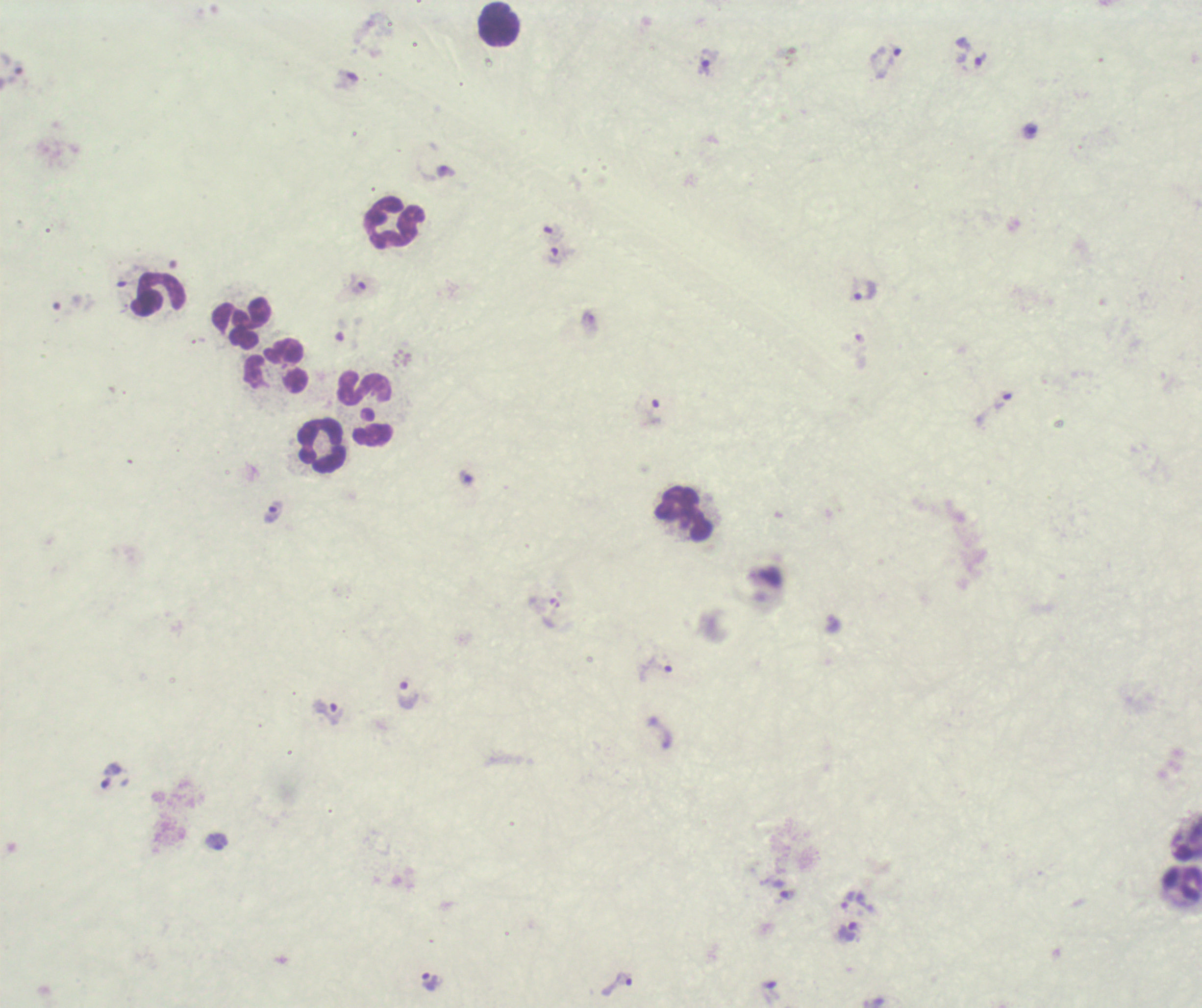
coordinate format = approximate object centers, in pixels from the top-left corner
trophozoite locations = (x=981, y=61), (x=886, y=62), (x=706, y=63), (x=1029, y=131), (x=445, y=172), (x=555, y=255), (x=357, y=285), (x=865, y=290), (x=1002, y=401), (x=651, y=412), (x=466, y=478), (x=273, y=512), (x=656, y=670), (x=407, y=695), (x=329, y=712), (x=111, y=776), (x=216, y=842), (x=787, y=895), (x=847, y=900), (x=847, y=933), (x=430, y=983), (x=617, y=984)
leukocyte locations = (x=498, y=24), (x=394, y=222), (x=156, y=294), (x=241, y=324), (x=275, y=367), (x=363, y=388), (x=373, y=435), (x=323, y=445), (x=684, y=514), (x=1180, y=884)
coloration quality = bad
preparation = thick blood film
stain = Romanowsky
result = malaria parasites identified
magnification = 100x
background quality = unsatisfactory
field of view = single
image size = 1202×1008 pixels
context = previously used in a real diagnosis